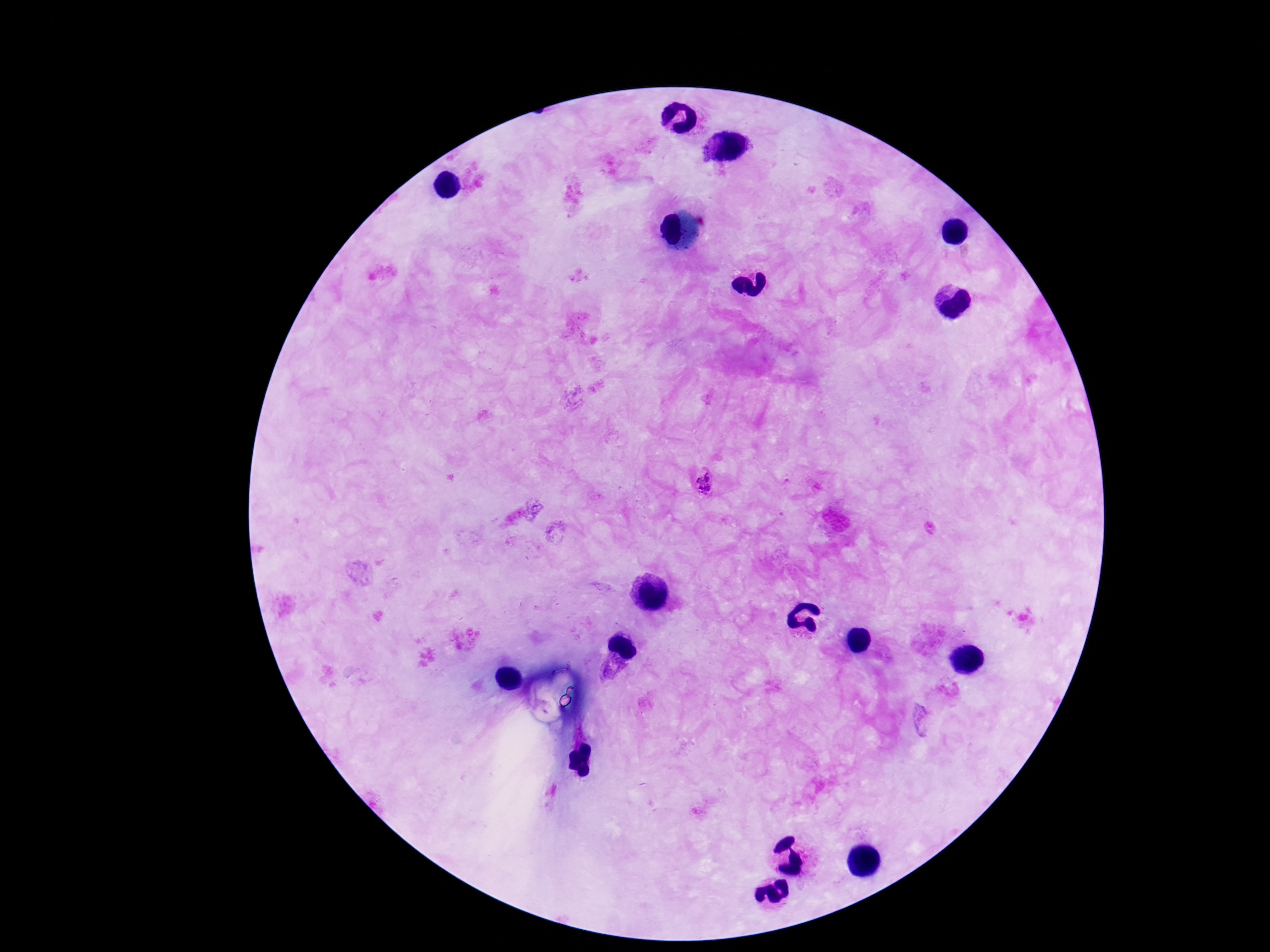
Approximate object centers, in pixels from the top-left corner. Plasmodium parasite locations: (x=705, y=483), (x=612, y=668), (x=921, y=721). Thick blood smear. Image is 1270×952 pixels. 100x magnification. Giemsa-stained preparation. Patient malaria status: positive. Photographed through the microscope eyepiece with a smartphone camera. Single field of view.